Comment on the morphology of the erythrocytes.
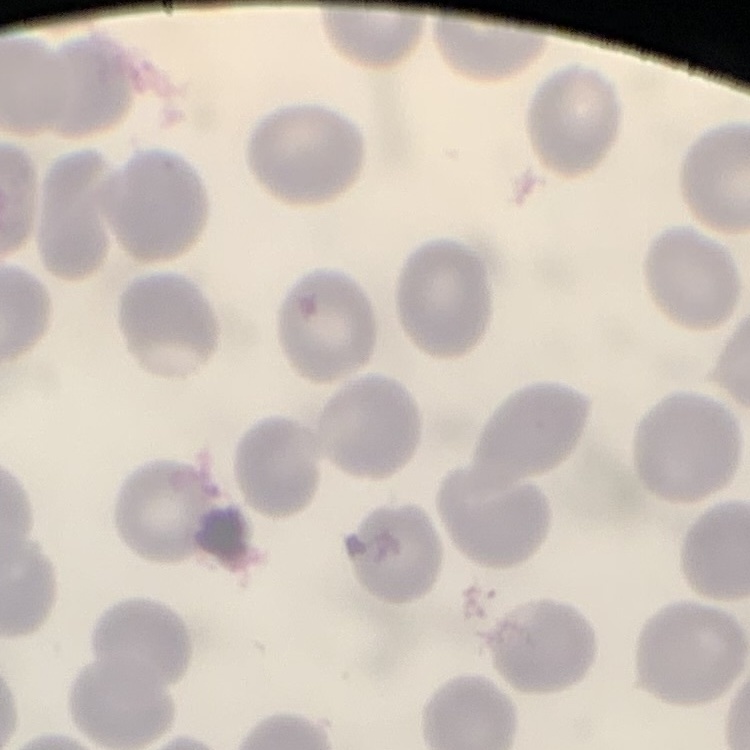

No rouleaux formation.

Summary:
  - Image type: one tile cut from a larger photomicrograph
  - Preparation: thin blood smear
  - Stain: Field's or Giemsa